Locate every uninfected red blood cell.
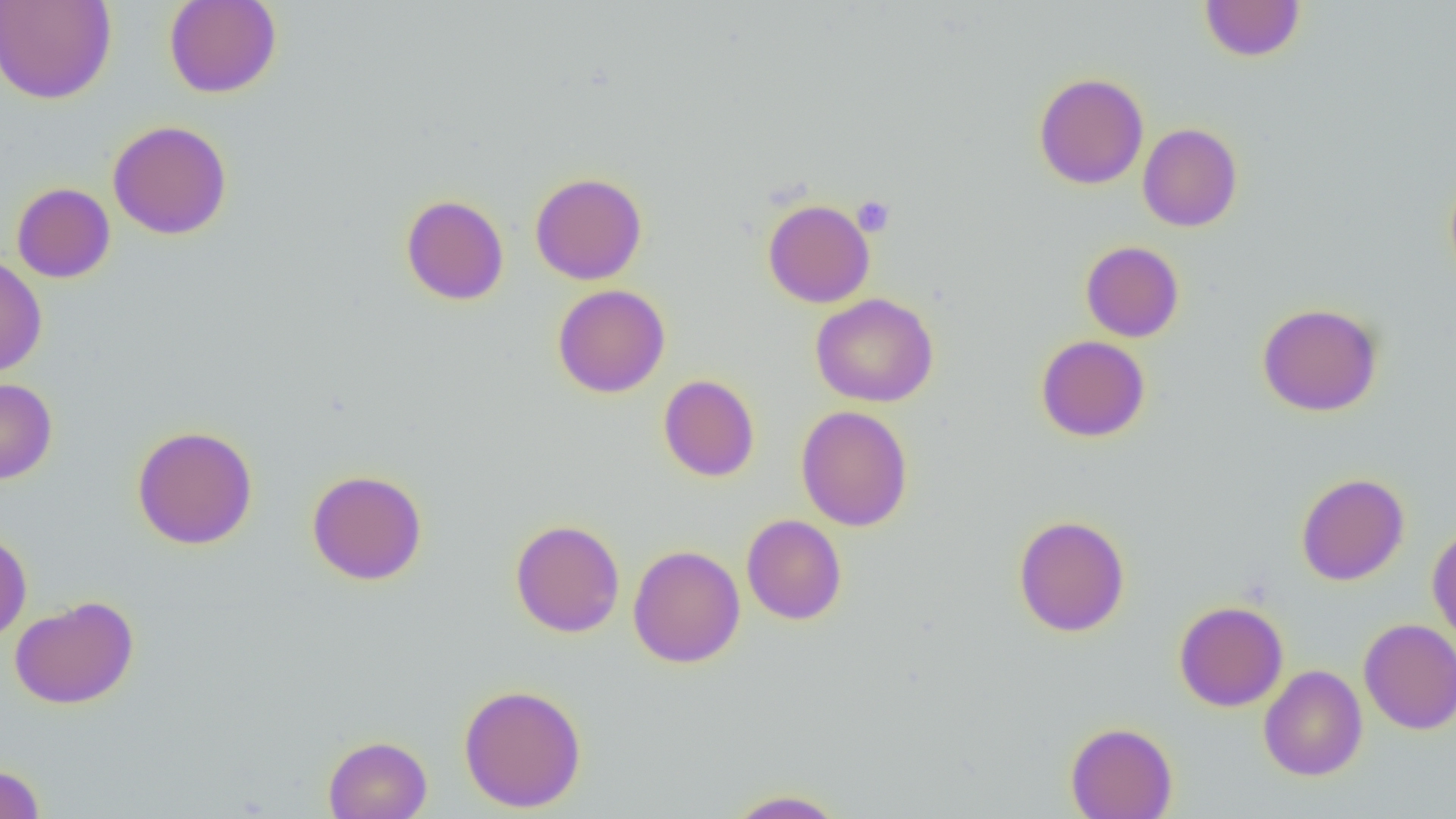
Approximate bounding boxes as named x1/y1/x2/y2 corners in pixels.
Uninfected red blood cells: (x1=0, y1=0, x2=116, y2=104), (x1=163, y1=0, x2=282, y2=98), (x1=1199, y1=1, x2=1306, y2=62), (x1=1033, y1=72, x2=1149, y2=190), (x1=108, y1=120, x2=232, y2=240), (x1=1137, y1=123, x2=1243, y2=232), (x1=530, y1=172, x2=647, y2=284), (x1=1444, y1=172, x2=1456, y2=290), (x1=12, y1=182, x2=116, y2=283), (x1=400, y1=194, x2=509, y2=305), (x1=762, y1=198, x2=875, y2=308), (x1=1080, y1=240, x2=1184, y2=342), (x1=0, y1=256, x2=47, y2=376), (x1=552, y1=284, x2=670, y2=398), (x1=810, y1=292, x2=939, y2=408), (x1=1257, y1=302, x2=1384, y2=416), (x1=1036, y1=335, x2=1150, y2=442), (x1=658, y1=374, x2=760, y2=482), (x1=0, y1=378, x2=58, y2=484), (x1=795, y1=405, x2=913, y2=531), (x1=131, y1=425, x2=258, y2=550), (x1=307, y1=469, x2=428, y2=586), (x1=1296, y1=473, x2=1410, y2=585), (x1=741, y1=514, x2=847, y2=625), (x1=1012, y1=514, x2=1130, y2=637), (x1=510, y1=519, x2=625, y2=638), (x1=1426, y1=525, x2=1456, y2=645), (x1=0, y1=530, x2=32, y2=641), (x1=629, y1=545, x2=746, y2=668), (x1=9, y1=595, x2=139, y2=709), (x1=1174, y1=600, x2=1289, y2=712), (x1=1359, y1=618, x2=1456, y2=735), (x1=1258, y1=665, x2=1367, y2=781), (x1=457, y1=683, x2=587, y2=813), (x1=1065, y1=721, x2=1177, y2=819), (x1=323, y1=735, x2=432, y2=819), (x1=0, y1=763, x2=45, y2=819), (x1=723, y1=788, x2=849, y2=818).

slide-level diagnosis = negative for blood parasites
platelet locations = approximate bounding boxes as named x1/y1/x2/y2 corners in pixels: (x1=852, y1=196, x2=895, y2=237)
modality = light microscopy
preparation = thin blood smear
magnification = 1000x
image size = 1456×819 pixels
field of view = one of a larger specimen